Classify this cell by malaria status.
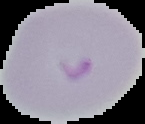

It is parasitized.

{
  "image_type": "segmented cell region with the area outside set to black",
  "image_size": "145×124 pixels",
  "preparation": "thin blood film"
}